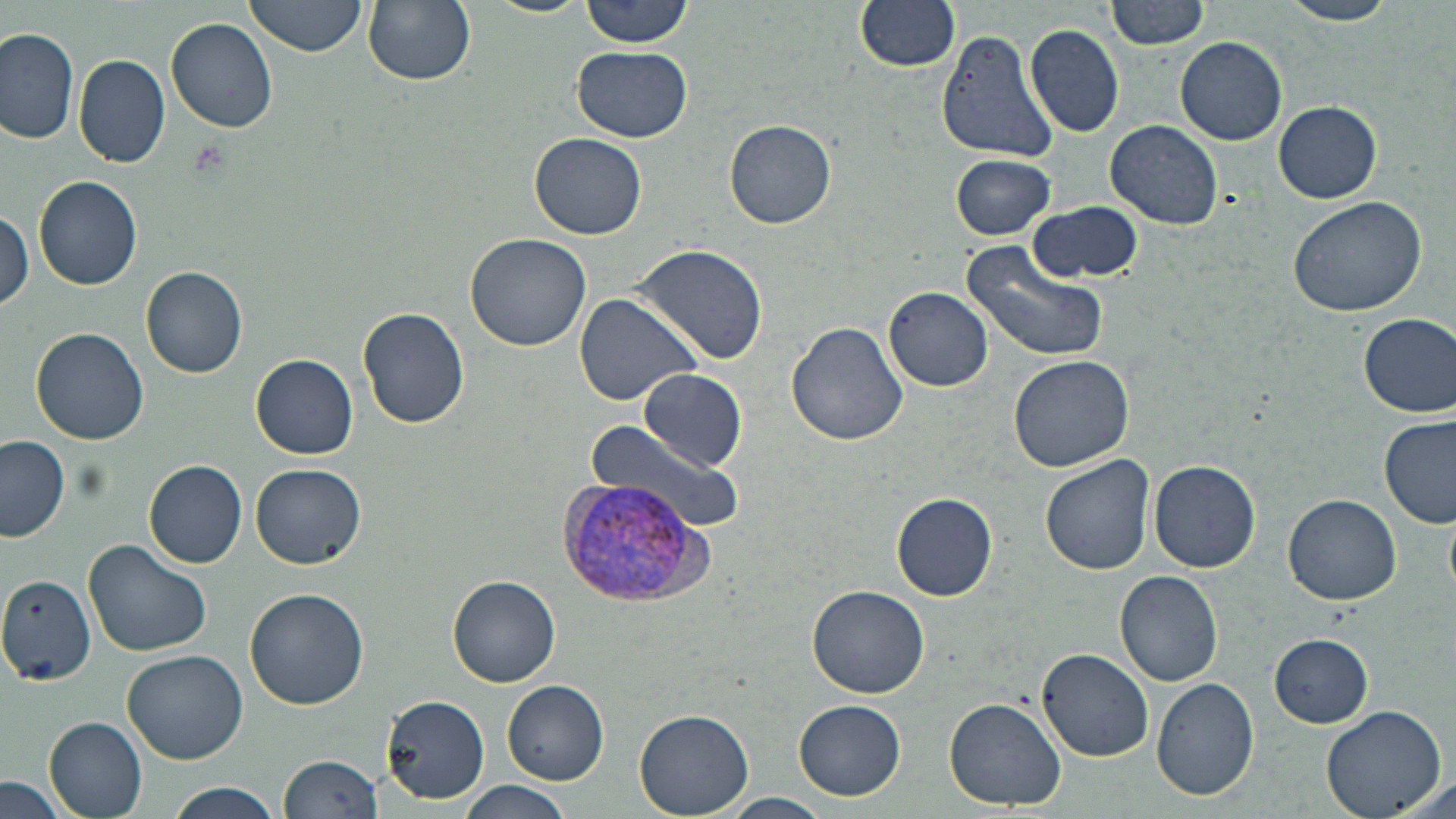
Summary:
  - Coordinate format: approximate bounding boxes as (x1,y1)-(x2,y2) corner pairs in pixels
  - Plasmodium vivax-infected red blood cell locations: (557,477)-(709,609)
  - Uninfected red blood cell locations: (246,0)-(366,57), (364,0)-(476,86), (483,0)-(593,18), (580,0)-(696,47), (853,0)-(960,73), (1105,0)-(1211,50), (1277,0)-(1401,26), (166,18)-(279,133), (1025,23)-(1124,138), (937,26)-(1060,164), (0,29)-(79,145), (1174,36)-(1287,146), (572,44)-(692,143), (75,54)-(170,168), (1273,101)-(1382,203), (725,119)-(837,229), (1105,120)-(1224,232), (529,132)-(647,240), (949,153)-(1057,241), (33,175)-(142,290), (1287,193)-(1427,318), (1028,202)-(1144,284), (0,206)-(31,310), (466,234)-(592,353), (629,242)-(769,365), (958,242)-(1110,362), (141,266)-(248,378), (885,287)-(993,391), (573,292)-(704,407), (357,307)-(470,429), (1358,313)-(1456,417), (787,321)-(910,446), (30,326)-(150,445), (251,353)-(359,458), (1009,356)-(1133,471), (637,368)-(748,472), (1380,415)-(1455,528), (586,418)-(742,538), (1,435)-(69,542), (1040,454)-(1155,576), (143,459)-(247,567), (1148,460)-(1261,572), (251,464)-(367,570), (892,493)-(996,600), (1284,494)-(1402,605), (82,541)-(213,657), (1115,571)-(1223,686), (0,573)-(97,686), (448,576)-(559,686), (807,583)-(930,697), (243,587)-(369,710), (1268,633)-(1376,728), (122,649)-(249,765), (1036,649)-(1154,762), (1151,678)-(1260,803), (502,679)-(611,785), (381,693)-(488,805), (944,696)-(1068,809), (794,699)-(905,798), (1319,704)-(1448,819), (634,710)-(755,819), (44,716)-(150,817), (279,755)-(386,819), (0,777)-(71,819), (460,779)-(574,819), (163,781)-(283,819), (721,793)-(832,819)
  - Platelet locations: (186,138)-(231,181)
  - Slide-level diagnosis: Plasmodium vivax
  - Magnification: 1000x
  - Field of view: single
  - Preparation: thin blood smear
  - Image size: 1456×819 pixels
  - Stain: May-Grünwald-Giemsa
  - Modality: light microscopy